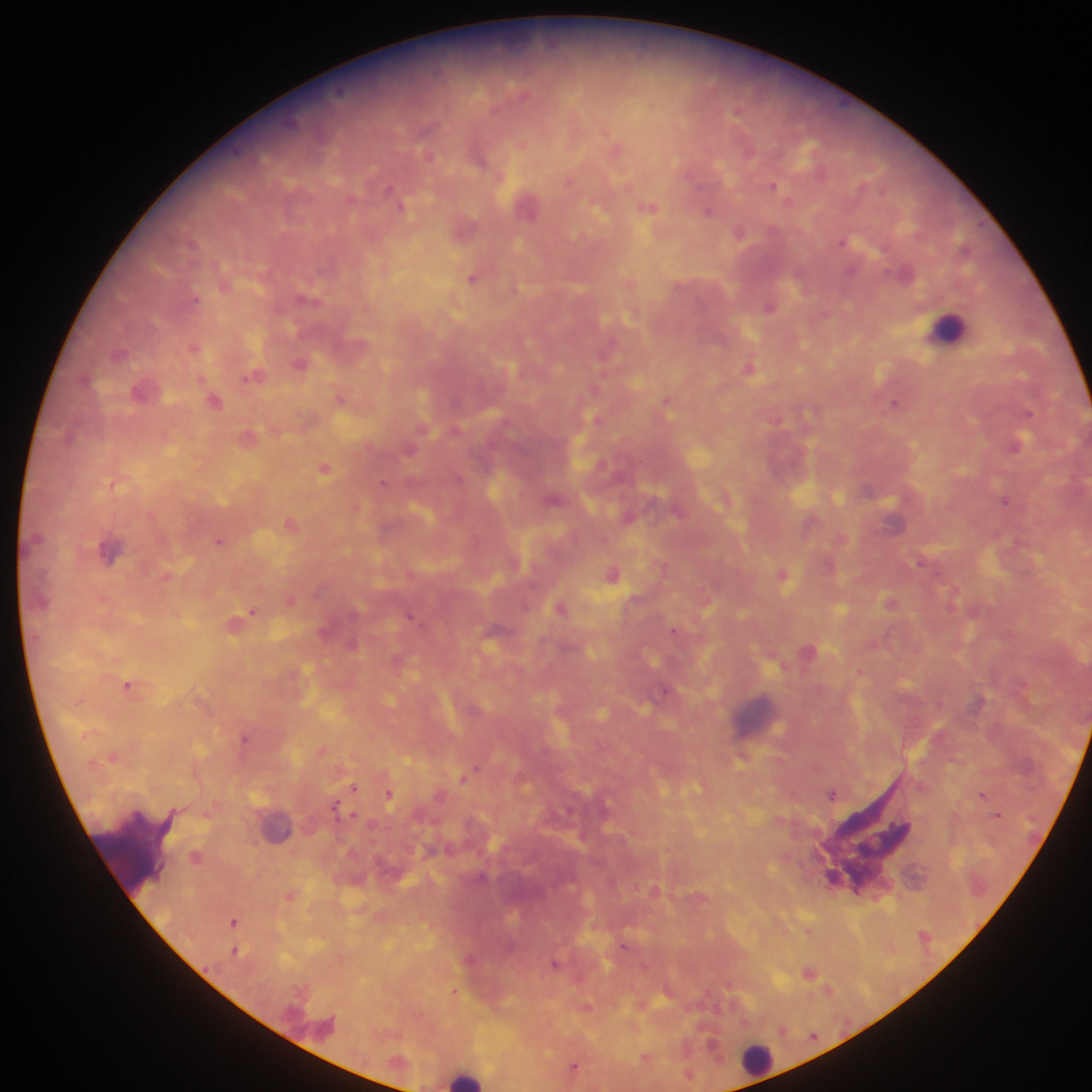

Approximate centers as x y in pixels. Leukocyte locations: 948 328; 275 825; 134 854; 756 1060; 466 1077. Malaria parasite locations: 737 111; 522 143; 617 148; 570 180; 773 185; 528 203; 402 207; 649 207; 709 210; 464 228; 740 232; 907 272; 474 278; 310 299; 770 306; 195 346; 119 353; 301 364; 750 368; 255 377; 595 388; 144 390; 342 398; 215 400; 667 401; 895 403; 598 419; 250 436; 1017 443; 410 450; 324 467; 112 482; 383 482; 553 499; 1005 500; 356 506; 896 521; 291 524; 843 537; 221 540; 109 550; 922 562; 664 566; 612 573; 783 574; 168 576; 291 600; 890 602; 562 608; 253 611; 411 616; 234 623; 675 630; 352 644; 809 651; 860 671; 129 684; 667 691; 246 738; 322 750; 114 756; 476 767; 466 775; 355 787; 389 793; 832 794; 983 794; 337 805; 207 814; 997 814; 197 856; 655 889; 290 895; 234 921; 810 930; 624 945; 235 950; 556 964; 808 971; 828 990; 455 992; 587 1007; 646 1057; 574 1066; 690 1074. Thick blood film. Mobile-phone photograph taken through the microscope. Sample from Ghana. Image is 1092×1092 pixels. Single field of view.